Name the parasite shown.
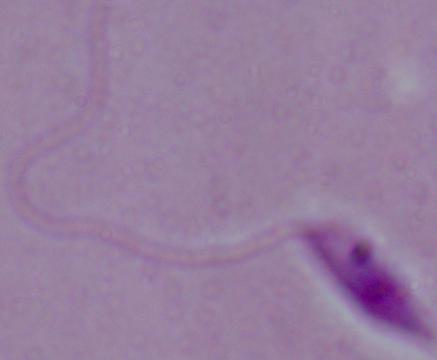
Leishmania.

Summary:
  - Magnification: 1000x
  - Modality: micrograph